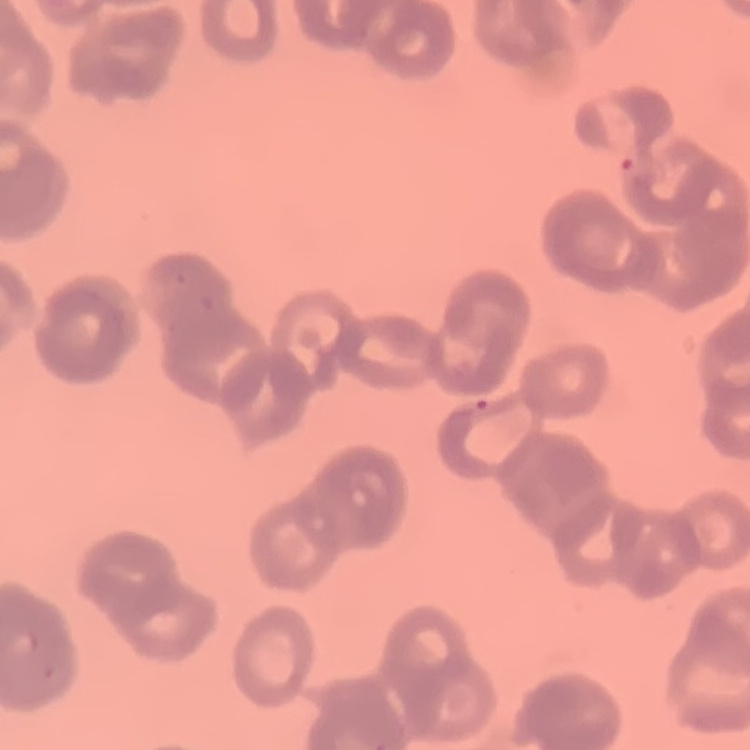

Summary:
  - Red blood cell morphology: rouleaux formation
  - Stain: Field's or Giemsa
  - Preparation: thin peripheral smear
  - Image type: square crop of a larger photomicrograph